Classify this cell by malaria status.
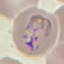
Parasitized.

Acquired by smartphone through the microscope eyepiece. Thin blood smear. Giemsa stain. Cell patch, automatically extracted from a larger field of view and resized to 64 × 64 pixels.